State the preparation type.
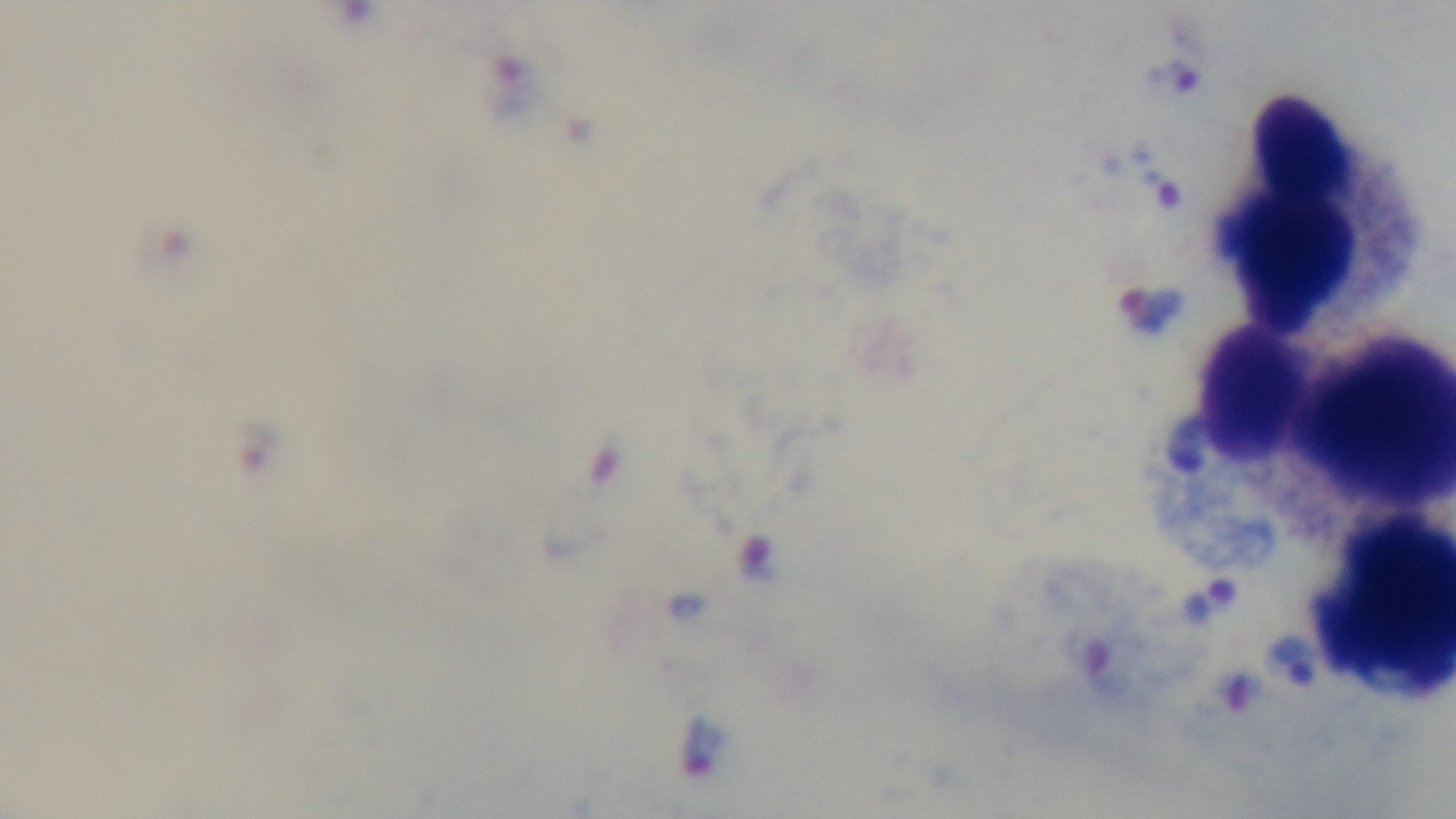
A thick smear.

{
  "modality": "light microscopy",
  "capture": "mounted 4K digital camera",
  "stain": "Giemsa",
  "malaria_status": "positive",
  "field_of_view": "single",
  "objective": "100x oil immersion"
}